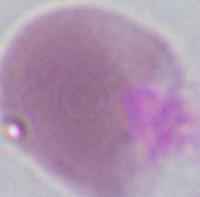

identification: red blood cell
magnification: 1000x
modality: micrograph